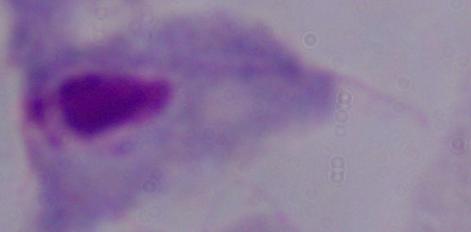
A trichomonad is shown. Captured at 1000x magnification. Photomicrograph.